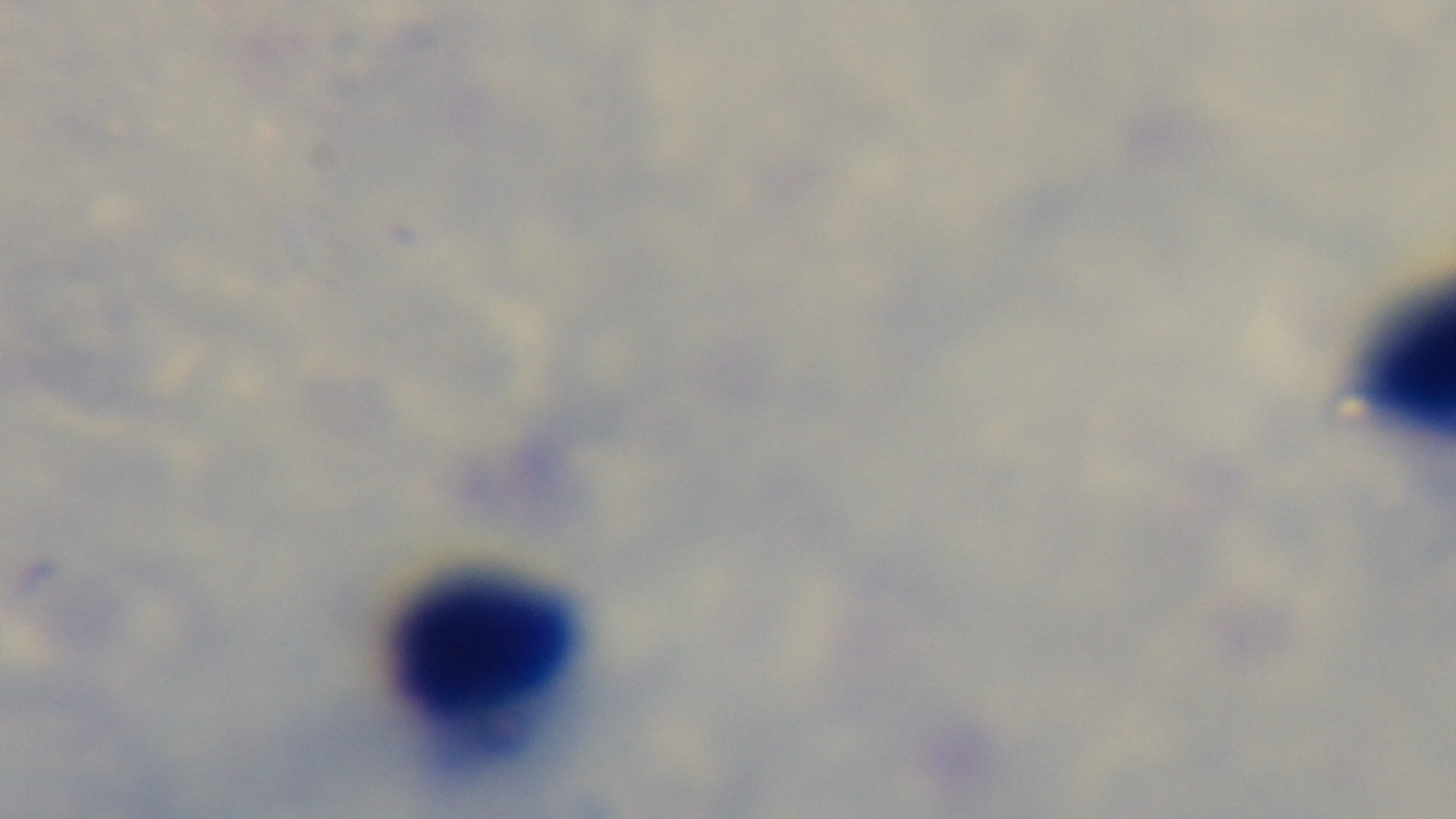
Summary:
  - Objective: 100x oil immersion
  - Malaria status: negative
  - Preparation: thick smear
  - Stain: Giemsa
  - Field of view: one from the slide
  - Capture: mounted 4K digital camera
  - Modality: light microscopy